Report the malaria status of this cell.
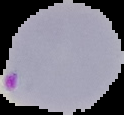

It is parasitized.

Summary:
  - Preparation: thin blood smear
  - Image size: 124×115 pixels
  - Image type: cell region segmented out of the field of view; surrounding area masked to black